Point out each malaria parasite and each leukocyte.
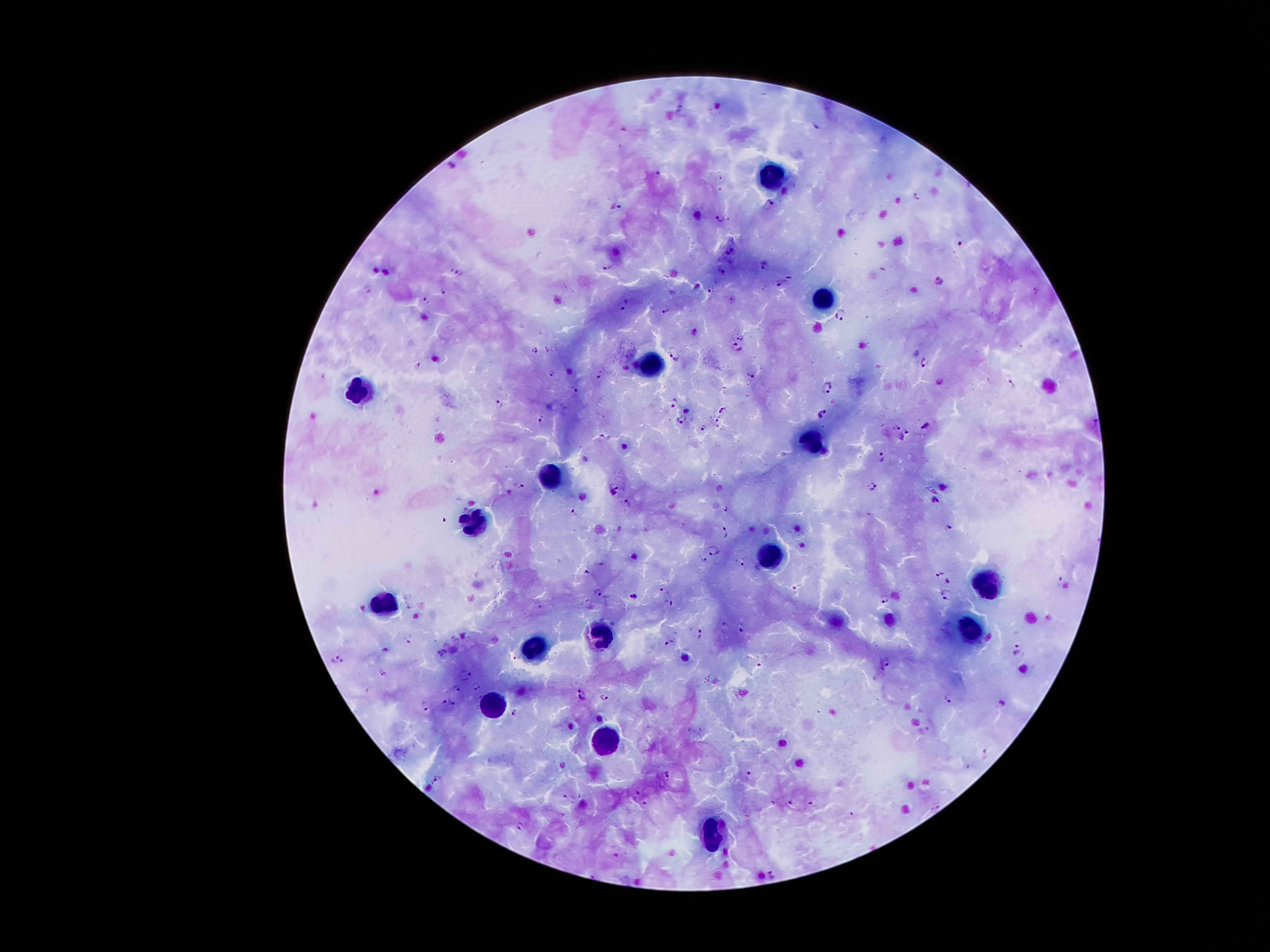

Approximate object centers, in pixels from the top-left corner.
Malaria parasites: (x=452, y=164), (x=915, y=196), (x=770, y=205), (x=618, y=207), (x=721, y=218), (x=960, y=241), (x=732, y=249), (x=763, y=265), (x=607, y=266), (x=721, y=269), (x=459, y=272), (x=790, y=275), (x=938, y=280), (x=780, y=282), (x=712, y=287), (x=444, y=291), (x=425, y=299), (x=623, y=305), (x=667, y=309), (x=839, y=313), (x=739, y=338), (x=735, y=348), (x=536, y=350), (x=674, y=353), (x=926, y=361), (x=418, y=365), (x=555, y=372), (x=600, y=373), (x=751, y=376), (x=827, y=383), (x=1012, y=383), (x=574, y=391), (x=674, y=401), (x=499, y=404), (x=723, y=408), (x=718, y=412), (x=822, y=414), (x=540, y=418), (x=681, y=419), (x=715, y=419), (x=1096, y=424), (x=704, y=426), (x=927, y=426), (x=896, y=427), (x=905, y=431), (x=604, y=435), (x=882, y=457), (x=613, y=485), (x=521, y=486), (x=871, y=488), (x=936, y=500), (x=627, y=502), (x=726, y=509), (x=572, y=512), (x=947, y=527), (x=724, y=530), (x=712, y=551), (x=704, y=560), (x=740, y=560), (x=587, y=572), (x=939, y=574), (x=948, y=580), (x=1060, y=581), (x=797, y=587), (x=665, y=589), (x=598, y=592), (x=945, y=592), (x=634, y=595), (x=884, y=598), (x=670, y=603), (x=725, y=624), (x=741, y=628), (x=698, y=632), (x=669, y=642), (x=1017, y=649), (x=341, y=657), (x=885, y=663), (x=382, y=672), (x=466, y=674), (x=477, y=686), (x=457, y=687), (x=582, y=695), (x=948, y=696), (x=605, y=698), (x=445, y=701), (x=425, y=704), (x=453, y=704), (x=515, y=712), (x=667, y=774), (x=749, y=775), (x=435, y=778), (x=637, y=793), (x=790, y=801), (x=646, y=802), (x=812, y=802), (x=520, y=826), (x=773, y=874).
Leukocytes: (x=771, y=180), (x=828, y=302), (x=653, y=368), (x=356, y=392), (x=810, y=439), (x=554, y=474), (x=474, y=518), (x=779, y=559), (x=986, y=583), (x=378, y=601), (x=969, y=626), (x=603, y=633), (x=534, y=644), (x=496, y=706), (x=605, y=744), (x=711, y=832).

One field from this slide. Patient malaria status: infected with Plasmodium falciparum. 100x magnification. Thick blood smear. Giemsa stain. Photographed through the microscope eyepiece with a smartphone camera. Image is 1270×952 pixels.